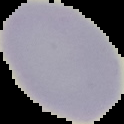
Summary:
  - Result: no malaria parasites detected
  - Preparation: thin blood smear
  - Image size: 124×124 pixels
  - Image type: segmented cell region with the area outside set to black